Name the parasite shown.
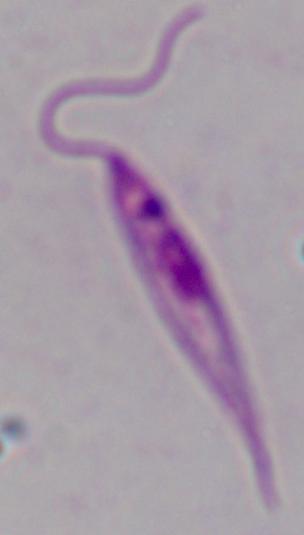
Leishmania.

Summary:
  - Modality: photomicrograph
  - Magnification: 1000x